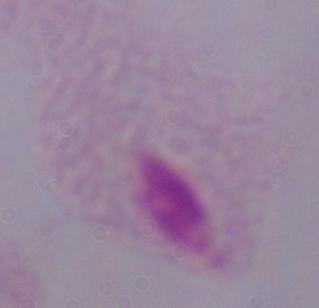
Photomicrograph. A trichomonad is shown. 1000x magnification.